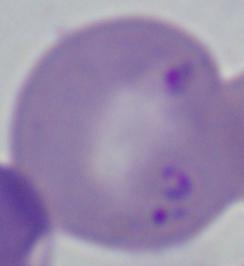

Summary:
  - Magnification: 1000x
  - Identification: Babesia
  - Modality: micrograph